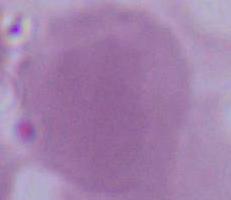
Captured at 1000x magnification. Photomicrograph. A red blood cell is shown.